Give the extent of all Plasmodium malariae-infected red blood cells.
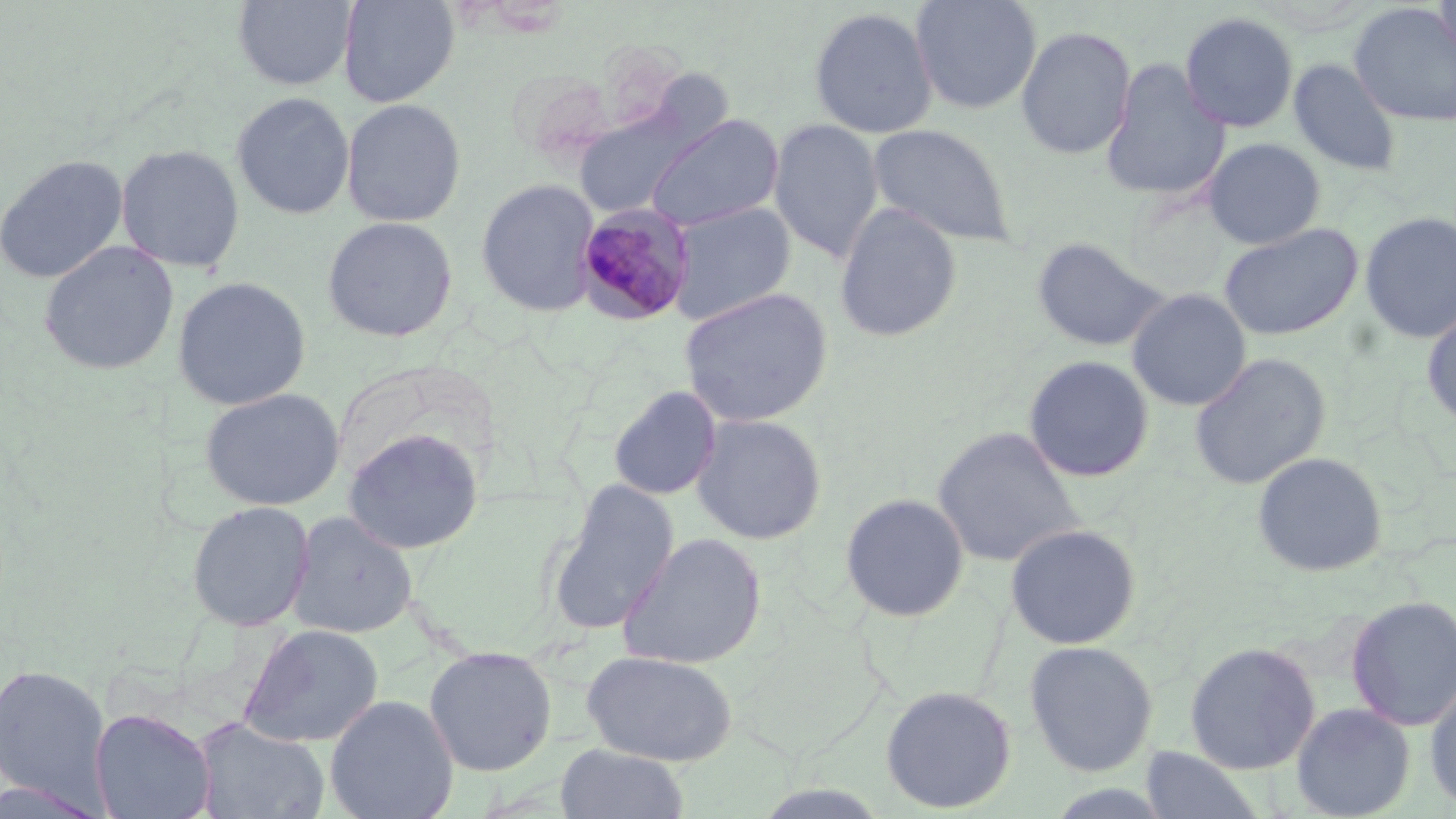
Approximate bounding boxes as [x1, y1, x2, y2] in pixels.
Plasmodium malariae-infected red blood cells: [574, 202, 696, 326].

slide-level diagnosis = Plasmodium malariae
modality = light microscopy
image size = 1456×819 pixels
preparation = thin blood film
field of view = one of a larger specimen
stain = May-Grünwald-Giemsa
magnification = 1000x
uninfected red blood cell locations = approximate bounding boxes as [x1, y1, x2, y2] in pixels: [234, 0, 357, 90], [338, 0, 458, 107], [910, 0, 1043, 115], [1433, 0, 1456, 63], [1349, 3, 1456, 126], [808, 6, 938, 139], [1179, 11, 1299, 133], [1015, 25, 1137, 160], [1288, 57, 1402, 176], [1100, 58, 1230, 202], [231, 92, 354, 219], [341, 98, 466, 227], [572, 101, 709, 219], [645, 113, 783, 232], [769, 118, 884, 263], [869, 122, 1016, 248], [1202, 138, 1326, 250], [115, 143, 245, 273], [0, 154, 128, 284], [476, 179, 601, 317], [667, 201, 796, 326], [833, 204, 963, 344], [1359, 211, 1456, 345], [321, 216, 458, 343], [1218, 222, 1363, 341], [1031, 236, 1171, 353], [38, 241, 179, 376], [172, 276, 311, 410], [678, 287, 833, 427], [1126, 288, 1252, 412], [1421, 306, 1456, 430], [1189, 353, 1331, 490], [1023, 354, 1154, 483], [608, 386, 722, 501], [199, 387, 345, 510], [691, 414, 827, 545], [932, 426, 1084, 568], [343, 427, 484, 555], [1252, 451, 1388, 577], [546, 479, 680, 635], [839, 492, 970, 622], [186, 500, 315, 632], [287, 511, 418, 639], [1004, 523, 1142, 650], [617, 532, 767, 670], [1345, 595, 1456, 731], [239, 623, 383, 748], [1023, 639, 1159, 777], [1184, 641, 1322, 775], [423, 645, 558, 776], [581, 650, 738, 765], [0, 662, 111, 807], [1424, 675, 1456, 811], [880, 684, 1017, 813], [325, 694, 458, 819], [1290, 702, 1416, 819], [89, 707, 217, 819], [192, 716, 330, 819], [554, 743, 689, 819], [1139, 746, 1265, 818], [0, 776, 114, 818]